State which parasite is depicted.
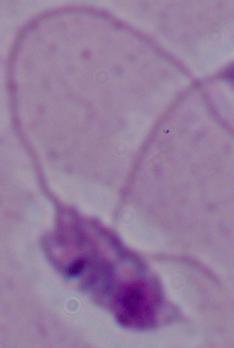

This is Leishmania.

Summary:
  - Magnification: 1000x
  - Modality: micrograph